Assess this cell for malaria.
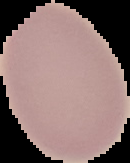
It is uninfected.

image type = segmented cell region on a black background
image size = 130×163 pixels
preparation = thin blood smear